Report the malaria status of this cell.
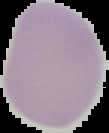
Uninfected.

The area outside the segmented cell region is set to black. From a thin blood smear. Image is 109×133 pixels.